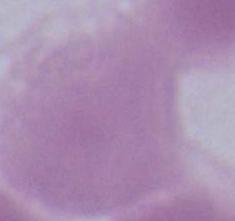

Photomicrograph. An erythrocyte is seen. Captured at 1000x magnification.